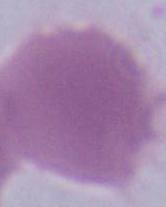

magnification = 1000x
identification = erythrocyte
modality = photomicrograph